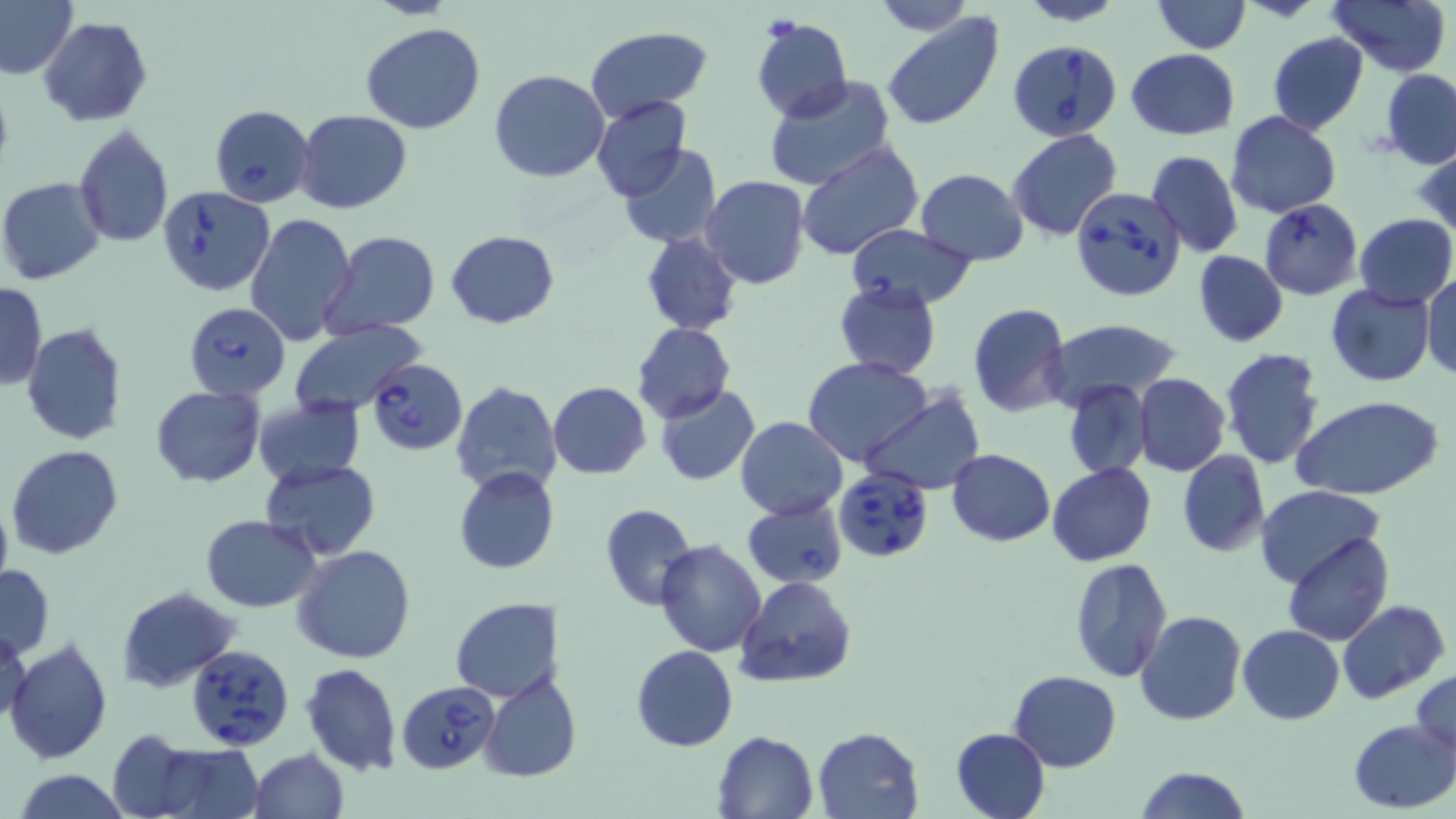

Summary:
  - Coordinate format: approximate bounding boxes as [x1, y1, x2, y2] in pixels
  - Babesia divergens-infected red blood cell locations: [1009, 39, 1122, 143], [209, 104, 316, 208], [157, 185, 275, 296], [1071, 185, 1186, 302], [1260, 198, 1362, 299], [844, 223, 978, 308], [184, 303, 290, 400], [367, 359, 466, 454], [835, 467, 935, 562], [742, 497, 848, 588], [187, 642, 293, 754], [397, 680, 499, 773]
  - Platelet locations: [767, 18, 799, 39]
  - Uninfected red blood cell locations: [1, 0, 79, 80], [868, 0, 974, 35], [1016, 0, 1127, 26], [1328, 0, 1450, 76], [1152, 1, 1250, 54], [881, 12, 1004, 132], [38, 16, 152, 127], [750, 17, 854, 123], [360, 22, 488, 133], [584, 25, 712, 125], [1267, 32, 1369, 136], [1125, 49, 1241, 140], [489, 69, 610, 182], [1380, 70, 1456, 165], [764, 76, 896, 189], [592, 95, 693, 202], [295, 110, 412, 213], [1226, 110, 1341, 218], [73, 124, 174, 247], [1007, 128, 1123, 241], [797, 142, 925, 262], [1414, 143, 1456, 237], [617, 144, 723, 249], [1146, 149, 1244, 259], [914, 169, 1029, 265], [0, 176, 106, 285], [701, 176, 810, 290], [243, 212, 357, 346], [1354, 215, 1455, 308], [323, 230, 440, 340], [446, 230, 560, 328], [641, 233, 742, 335], [1194, 251, 1288, 347], [1421, 274, 1455, 381], [833, 279, 941, 380], [0, 281, 47, 389], [1325, 283, 1434, 385], [968, 303, 1072, 417], [1042, 319, 1183, 412], [632, 322, 735, 423], [23, 323, 130, 446], [288, 324, 426, 417], [1219, 348, 1326, 469], [804, 357, 933, 466], [1133, 373, 1230, 476], [1063, 380, 1152, 480], [450, 381, 562, 497], [548, 381, 651, 478], [149, 384, 266, 487], [654, 384, 761, 486], [860, 392, 985, 493], [252, 395, 365, 490], [1291, 396, 1446, 501], [735, 417, 849, 520], [7, 445, 124, 560], [947, 448, 1055, 547], [1177, 450, 1270, 557], [259, 458, 381, 561], [1047, 463, 1157, 566], [454, 466, 558, 575], [1256, 485, 1386, 587], [0, 494, 13, 594], [599, 504, 697, 610], [199, 514, 321, 611], [1282, 533, 1394, 646], [654, 539, 767, 657], [293, 545, 416, 664], [1067, 558, 1173, 683], [0, 565, 54, 659], [736, 577, 854, 689], [116, 587, 240, 693], [450, 598, 560, 702], [1338, 600, 1449, 703], [1136, 611, 1247, 728], [1237, 624, 1346, 724], [1, 625, 31, 730], [6, 637, 112, 765], [631, 644, 738, 752], [301, 662, 401, 775], [1411, 667, 1456, 762], [1010, 670, 1121, 772], [479, 672, 582, 783], [1348, 718, 1455, 813], [812, 727, 923, 818], [951, 727, 1051, 819], [713, 729, 819, 818], [108, 731, 206, 816], [144, 741, 265, 818], [248, 747, 350, 818], [1133, 766, 1251, 819], [10, 770, 133, 818]
  - Slide-level diagnosis: Babesia divergens
  - Preparation: thin blood smear
  - Field of view: one of a larger specimen
  - Stain: May-Grünwald-Giemsa
  - Image size: 1456×819 pixels
  - Modality: optical microscopy
  - Magnification: 1000x